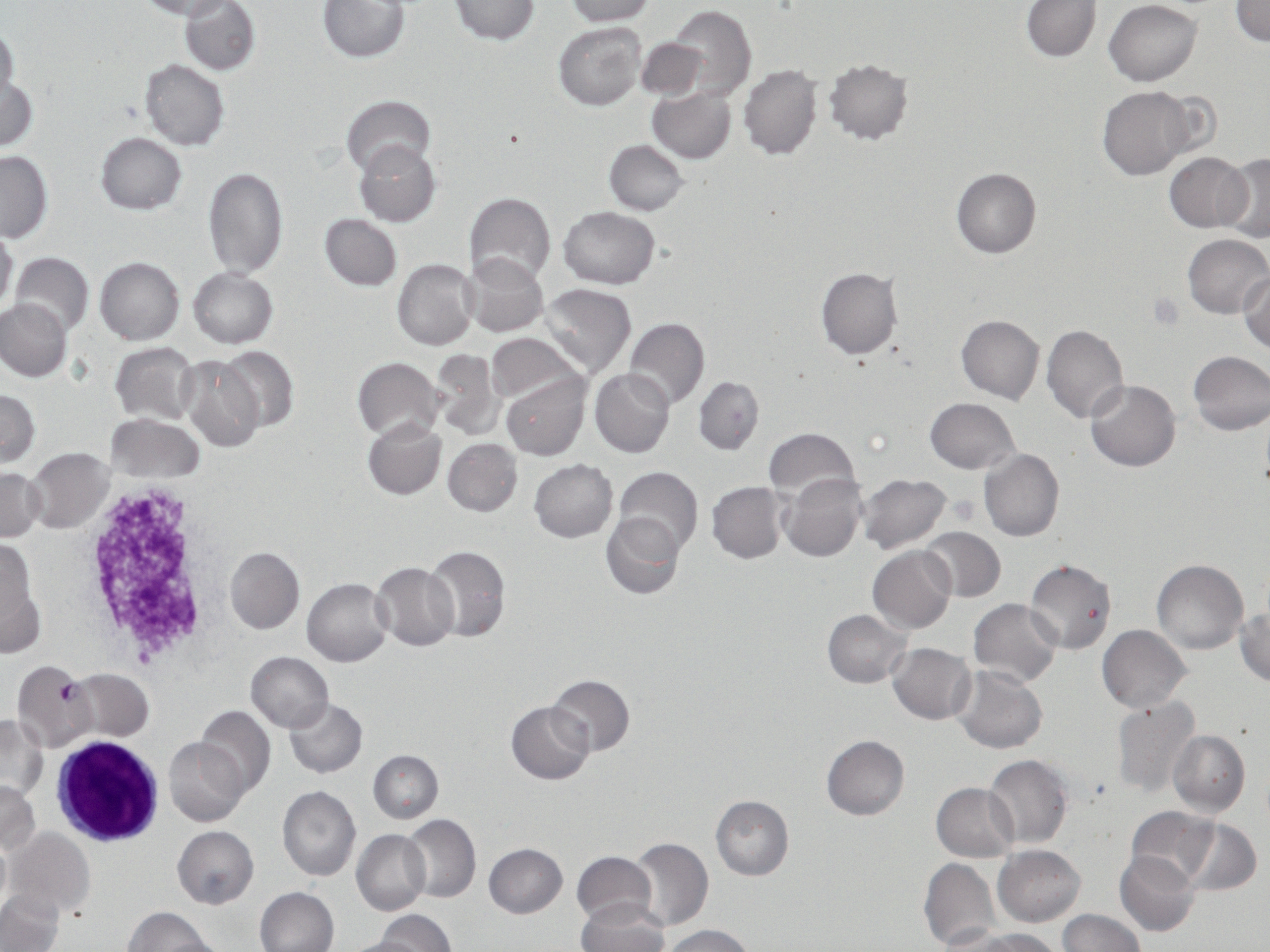

{
  "slide_level_diagnosis": "Plasmodium falciparum",
  "magnification": "1000x",
  "platelet_locations": "approximate bounding boxes as (x1,y1)-(x2,y2) corner pairs in pixels: (1148,292)-(1186,331)",
  "preparation": "thin blood smear",
  "stain": "May-Grünwald-Giemsa",
  "plasmodium_falciparum_infected_red_blood_cell_locations": "approximate bounding boxes as (x1,y1)-(x2,y2) corner pairs in pixels: (11,661)-(97,751)",
  "image_size": "1270×952 pixels",
  "uninfected_red_blood_cell_locations": "approximate bounding boxes as (x1,y1)-(x2,y2) corner pairs in pixels: (318,0)-(410,62), (450,0)-(539,44), (564,0)-(655,24), (1022,0)-(1100,61), (1231,0)-(1270,47), (137,1)-(232,20), (180,1)-(260,75), (1103,1)-(1202,85), (667,5)-(755,100), (553,21)-(645,110), (0,26)-(18,103), (636,38)-(708,99), (823,58)-(913,144), (139,59)-(230,149), (739,65)-(822,160), (2,78)-(38,152), (1097,86)-(1197,180), (648,87)-(736,162), (342,94)-(435,178), (95,132)-(186,215), (356,139)-(441,226), (604,140)-(688,216), (0,150)-(51,241), (1218,151)-(1270,244), (1165,153)-(1252,232), (202,168)-(287,278), (952,168)-(1041,258), (463,192)-(556,285), (559,206)-(660,289), (319,213)-(401,290), (0,227)-(17,317), (1183,233)-(1270,318), (9,252)-(93,335), (461,253)-(548,337), (95,256)-(184,343), (393,260)-(478,351), (188,267)-(277,347), (816,268)-(903,359), (1239,273)-(1270,353), (539,283)-(637,377), (0,298)-(71,381), (956,315)-(1044,404), (623,317)-(709,409), (1042,325)-(1129,424), (485,333)-(583,405), (109,343)-(199,423), (218,346)-(299,431), (430,348)-(503,439), (1187,351)-(1269,435), (179,355)-(264,453), (352,356)-(443,441), (590,368)-(675,457), (501,373)-(588,461), (693,376)-(764,455), (1085,380)-(1181,471), (0,389)-(40,466), (924,398)-(1021,474), (106,414)-(204,484), (362,417)-(446,500), (762,428)-(859,500), (442,438)-(522,516), (25,447)-(114,532), (979,449)-(1064,542), (529,459)-(617,542), (1,466)-(44,540), (614,467)-(704,555), (781,472)-(866,563), (855,473)-(953,554), (706,481)-(789,564), (602,512)-(685,599), (920,527)-(1005,602), (0,537)-(41,646), (421,544)-(511,643), (225,546)-(304,634), (867,546)-(956,633), (1025,558)-(1117,653), (1153,560)-(1249,654), (371,561)-(460,651), (303,577)-(393,667), (969,598)-(1061,687), (1236,605)-(1269,687), (823,610)-(912,688), (1097,626)-(1191,711), (888,643)-(976,724), (246,651)-(333,732), (950,664)-(1048,754), (68,669)-(153,740), (546,675)-(634,757), (1112,696)-(1201,798), (284,697)-(367,777), (507,701)-(595,785), (194,704)-(275,796), (0,715)-(45,799), (1168,729)-(1249,817), (821,735)-(909,820), (164,736)-(250,827), (368,749)-(443,824), (984,753)-(1072,848), (0,780)-(40,855), (930,782)-(1018,861), (278,785)-(361,881), (710,795)-(793,881), (1125,806)-(1221,886), (402,814)-(481,903), (1180,818)-(1262,895), (173,826)-(259,908), (6,827)-(94,919), (351,829)-(430,915), (0,838)-(11,916), (628,838)-(714,931), (484,843)-(568,918), (993,845)-(1085,926), (1114,850)-(1200,936), (571,851)-(656,926), (919,856)-(1001,952), (255,887)-(338,952), (0,890)-(64,952), (577,900)-(668,952), (122,907)-(215,951), (376,910)-(453,952), (1058,910)-(1146,952), (659,925)-(757,952), (965,928)-(1063,952), (338,936)-(425,952)",
  "white_blood_cell_locations": "approximate bounding boxes as (x1,y1)-(x2,y2) corner pairs in pixels: (51,740)-(166,847)",
  "field_of_view": "one of a larger specimen",
  "modality": "optical microscopy"
}